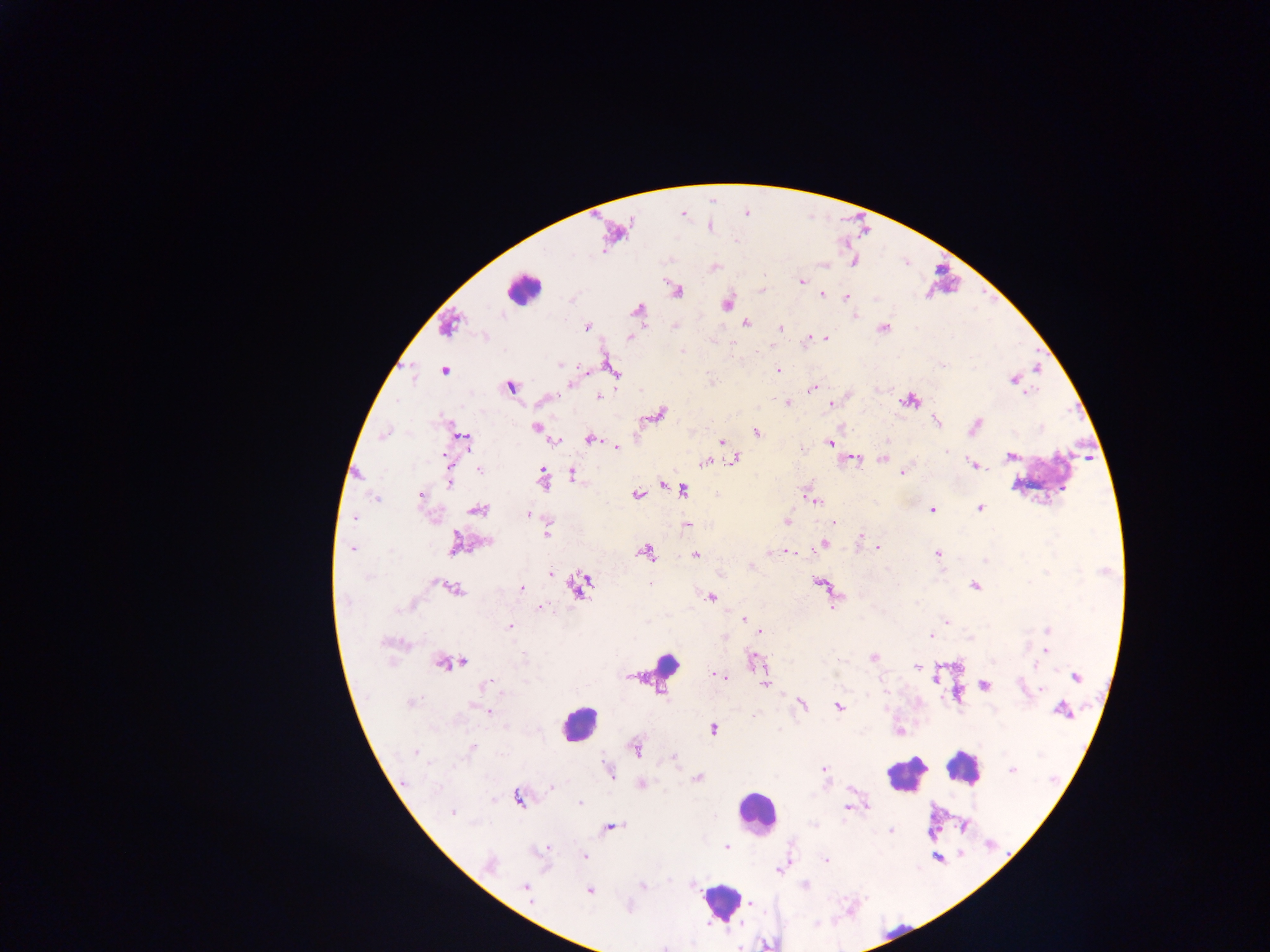

{
  "country": "Ghana",
  "leukocyte_locations": "approximate centers as (x, y) in pixels: (522, 287), (666, 663), (577, 724), (962, 768), (906, 774), (756, 812), (720, 902)",
  "malaria_parasite_locations": "approximate centers as (x, y) in pixels: (802, 281), (678, 291), (822, 295), (846, 297), (727, 303), (637, 310), (855, 316), (746, 323), (448, 326), (587, 327), (780, 328), (884, 328), (631, 337), (825, 338), (805, 341), (732, 343), (683, 350), (560, 365), (778, 370), (443, 371), (1012, 379), (570, 384), (510, 387), (811, 390), (1028, 393), (598, 397), (910, 400), (788, 403), (831, 403), (661, 413), (937, 421), (975, 426), (535, 427), (756, 432), (383, 434), (466, 439), (589, 439), (555, 441), (721, 442), (830, 443), (615, 448), (947, 451), (1011, 456), (735, 458), (882, 458), (853, 459), (704, 462), (972, 464), (480, 470), (571, 473), (903, 473), (542, 478), (450, 483), (663, 485), (683, 490), (421, 495), (636, 495), (375, 499), (812, 500), (979, 508), (478, 510), (932, 510), (527, 514), (356, 518), (787, 522), (834, 522), (687, 524), (547, 533), (861, 536), (455, 543), (487, 543), (823, 544), (877, 547), (353, 549), (645, 552), (791, 552), (768, 553), (695, 554), (937, 554), (550, 573), (435, 583), (650, 584), (578, 586), (975, 586), (521, 589), (456, 591), (711, 597), (834, 604), (539, 608), (743, 619), (947, 621), (509, 627), (1048, 630), (761, 631), (931, 635), (724, 637), (971, 638), (1046, 651), (874, 657), (753, 658), (838, 660), (464, 661), (442, 663), (917, 667), (717, 676), (724, 676), (1076, 677), (765, 684), (486, 685), (984, 686), (1040, 689), (410, 702), (801, 704), (839, 707), (1062, 710), (488, 711), (713, 729), (471, 748), (637, 750), (414, 752), (674, 757), (429, 764), (608, 768), (825, 770), (1012, 770), (697, 778), (641, 784), (551, 786), (518, 799), (579, 802), (867, 805), (846, 808), (452, 813), (612, 826), (891, 831), (726, 847), (541, 850), (585, 856), (826, 860), (489, 864), (780, 870), (643, 886), (805, 886), (526, 888), (589, 890), (750, 903), (628, 907), (664, 948)",
  "capture": "mobile-phone photograph through a microscope",
  "preparation": "thick blood film",
  "image_size": "1270×952 pixels",
  "field_of_view": "single"
}